Comment on the morphology of the erythrocytes.
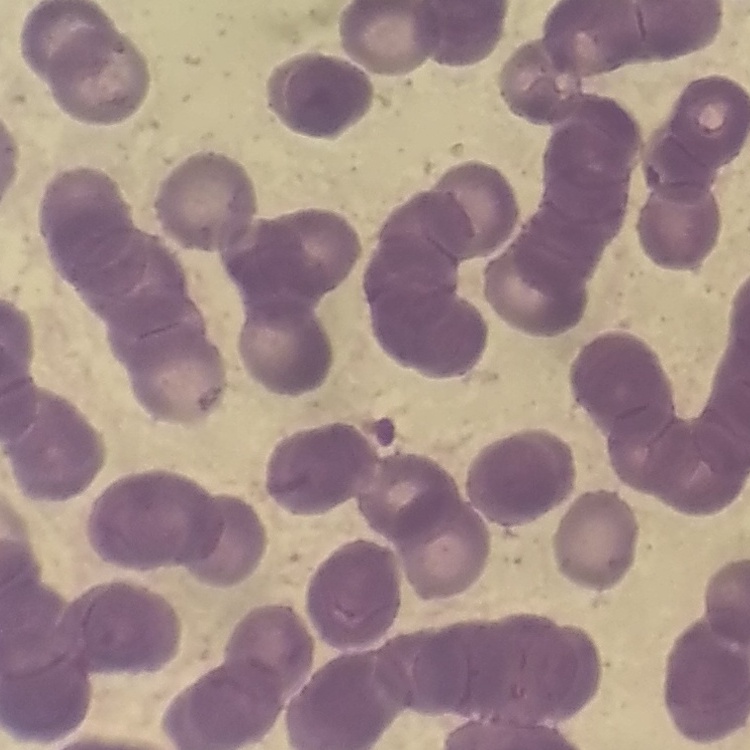

Rouleaux formation.

preparation = thin blood smear
image type = square crop of a larger photomicrograph
stain = Field's or Giemsa